Locate every Plasmodium ovale-infected red blood cell.
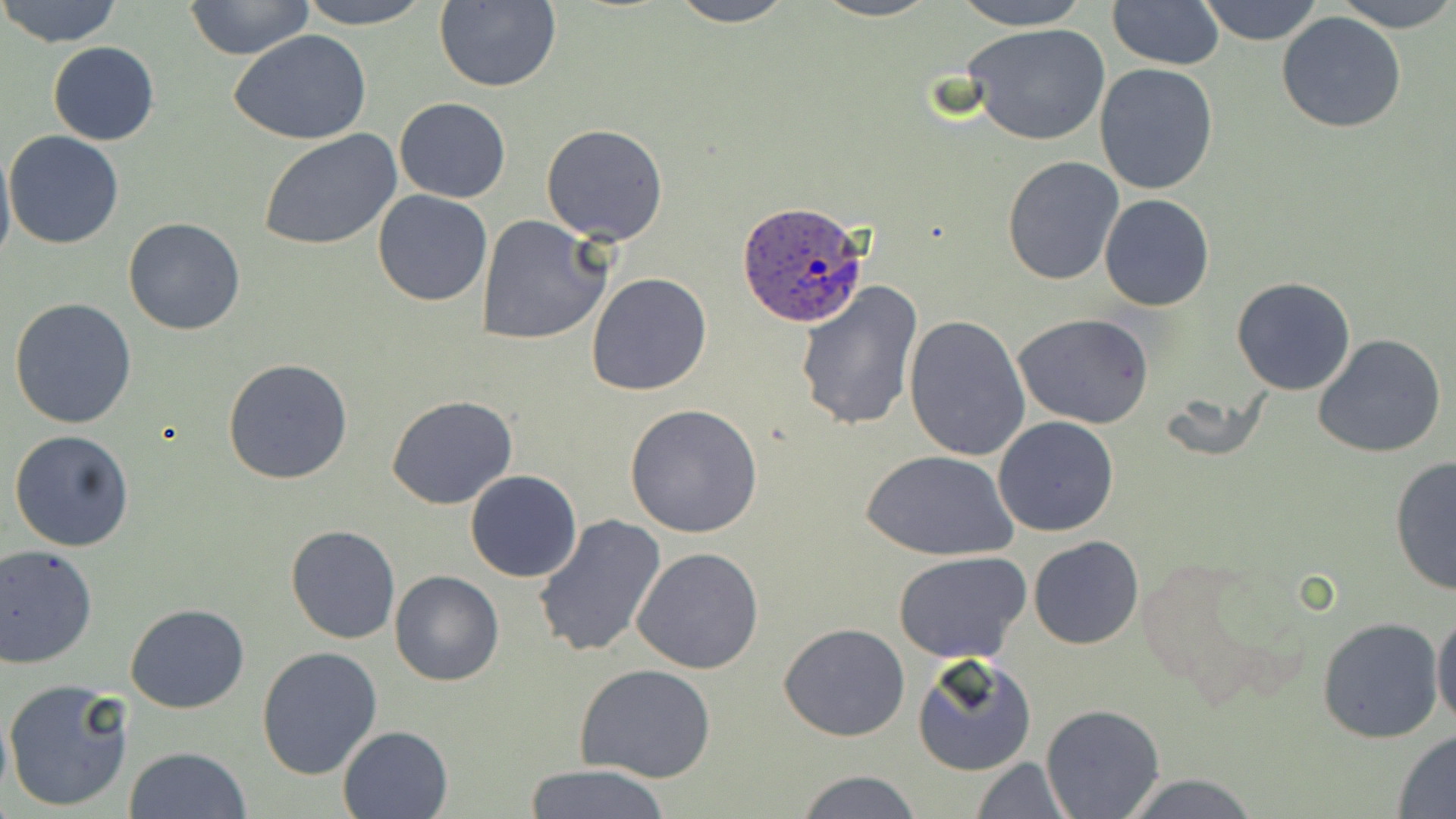

Approximate bounding boxes as named x1/y1/x2/y2 corners in pixels.
Plasmodium ovale-infected red blood cells: (x1=736, y1=200, x2=869, y2=327).

Summary:
  - Uninfected red blood cell locations: (x1=0, y1=0, x2=123, y2=48), (x1=182, y1=0, x2=316, y2=61), (x1=298, y1=0, x2=432, y2=28), (x1=667, y1=0, x2=796, y2=27), (x1=813, y1=0, x2=938, y2=22), (x1=950, y1=0, x2=1093, y2=29), (x1=1335, y1=0, x2=1456, y2=31), (x1=433, y1=1, x2=561, y2=91), (x1=1107, y1=1, x2=1224, y2=69), (x1=1195, y1=1, x2=1326, y2=45), (x1=1276, y1=11, x2=1407, y2=133), (x1=962, y1=22, x2=1111, y2=145), (x1=229, y1=29, x2=376, y2=147), (x1=48, y1=41, x2=159, y2=146), (x1=1093, y1=64, x2=1218, y2=195), (x1=393, y1=98, x2=510, y2=202), (x1=541, y1=123, x2=670, y2=245), (x1=258, y1=129, x2=401, y2=252), (x1=5, y1=130, x2=124, y2=249), (x1=0, y1=141, x2=15, y2=273), (x1=1002, y1=155, x2=1124, y2=285), (x1=372, y1=190, x2=493, y2=307), (x1=1099, y1=193, x2=1214, y2=312), (x1=476, y1=216, x2=611, y2=346), (x1=122, y1=217, x2=247, y2=335), (x1=585, y1=271, x2=713, y2=396), (x1=1231, y1=277, x2=1356, y2=395), (x1=797, y1=283, x2=924, y2=431), (x1=9, y1=298, x2=138, y2=430), (x1=1012, y1=312, x2=1155, y2=427), (x1=903, y1=315, x2=1030, y2=462), (x1=1313, y1=333, x2=1446, y2=459), (x1=221, y1=357, x2=353, y2=485), (x1=388, y1=394, x2=518, y2=510), (x1=624, y1=404, x2=766, y2=539), (x1=992, y1=416, x2=1120, y2=537), (x1=8, y1=428, x2=135, y2=552), (x1=864, y1=449, x2=1017, y2=562), (x1=1389, y1=454, x2=1455, y2=597), (x1=465, y1=470, x2=581, y2=582), (x1=534, y1=513, x2=665, y2=658), (x1=285, y1=526, x2=400, y2=645), (x1=1028, y1=536, x2=1144, y2=651), (x1=0, y1=543, x2=98, y2=668), (x1=632, y1=547, x2=764, y2=675), (x1=895, y1=550, x2=1031, y2=662), (x1=389, y1=571, x2=505, y2=687), (x1=124, y1=604, x2=250, y2=714), (x1=1431, y1=607, x2=1456, y2=733), (x1=1315, y1=616, x2=1444, y2=743), (x1=778, y1=622, x2=910, y2=742), (x1=255, y1=646, x2=383, y2=779), (x1=912, y1=654, x2=1037, y2=777), (x1=575, y1=663, x2=716, y2=784), (x1=3, y1=678, x2=134, y2=813), (x1=1041, y1=704, x2=1164, y2=817), (x1=337, y1=724, x2=454, y2=818), (x1=1393, y1=730, x2=1456, y2=817), (x1=122, y1=745, x2=253, y2=819), (x1=970, y1=756, x2=1073, y2=818), (x1=524, y1=763, x2=670, y2=819), (x1=793, y1=771, x2=926, y2=818), (x1=1120, y1=773, x2=1259, y2=817)
  - Slide-level diagnosis: Plasmodium ovale
  - Magnification: 1000x
  - Stain: May-Grünwald-Giemsa
  - Modality: optical microscopy
  - Field of view: single
  - Image size: 1456×819 pixels
  - Preparation: thin blood smear